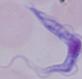

A trypanosome is seen. Micrograph. 1000x magnification.